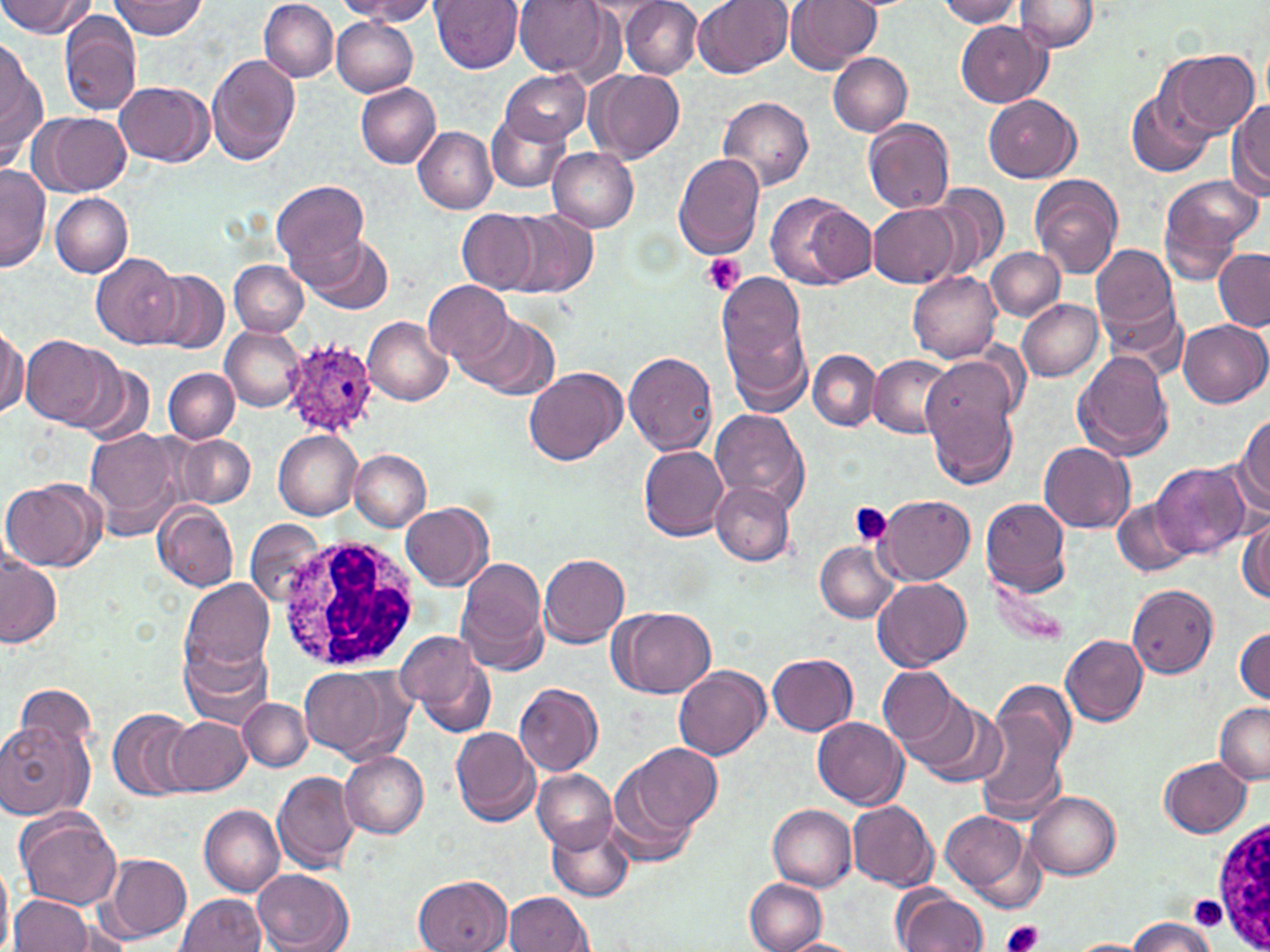

Summary:
  - Coordinate format: approximate bounding boxes as (x1, y1, x2, y2) in pixels
  - Plasmodium ovale-infected red blood cell locations: (283, 340, 379, 435)
  - Uninfected red blood cell locations: (0, 0, 93, 38), (111, 0, 206, 38), (258, 0, 339, 82), (338, 0, 441, 23), (433, 0, 524, 73), (513, 0, 612, 77), (693, 0, 792, 78), (785, 0, 879, 72), (936, 0, 1024, 27), (621, 1, 703, 79), (1014, 1, 1099, 53), (59, 14, 140, 116), (331, 18, 418, 96), (955, 20, 1051, 107), (1, 40, 46, 164), (1162, 50, 1260, 138), (207, 52, 301, 165), (827, 53, 912, 136), (498, 69, 590, 146), (587, 69, 685, 164), (115, 81, 213, 167), (356, 83, 441, 169), (1126, 88, 1214, 179), (983, 94, 1082, 182), (717, 95, 814, 192), (1228, 100, 1270, 199), (36, 112, 130, 196), (485, 113, 571, 193), (864, 118, 956, 213), (413, 126, 496, 212), (547, 147, 639, 232), (673, 154, 766, 258), (1, 165, 49, 273), (1029, 174, 1124, 278), (1158, 175, 1263, 267), (272, 180, 370, 280), (928, 184, 1008, 278), (765, 192, 868, 290), (49, 193, 133, 277), (868, 204, 961, 289), (457, 209, 539, 293), (507, 211, 598, 298), (307, 235, 394, 316), (1089, 243, 1180, 350), (986, 247, 1065, 320), (1213, 250, 1269, 331), (92, 252, 184, 349), (229, 260, 307, 335), (148, 270, 229, 354), (715, 271, 816, 419), (907, 272, 1002, 362), (423, 280, 516, 368), (1016, 298, 1105, 380), (460, 313, 559, 399), (364, 316, 452, 405), (1179, 320, 1269, 407), (0, 323, 26, 419), (221, 327, 303, 411), (19, 334, 117, 429), (808, 349, 881, 431), (1073, 350, 1174, 460), (623, 352, 719, 455), (924, 354, 1023, 442), (867, 355, 953, 438), (80, 360, 156, 445), (522, 365, 627, 465), (163, 366, 240, 443), (924, 386, 1019, 490), (710, 408, 810, 512), (1234, 413, 1270, 512), (86, 428, 183, 537), (273, 430, 361, 519), (179, 436, 254, 507), (1039, 441, 1136, 533), (639, 446, 728, 542), (349, 449, 429, 531), (1152, 463, 1249, 561), (1, 478, 104, 572), (710, 479, 794, 565), (877, 495, 974, 583), (980, 497, 1073, 596), (1112, 498, 1193, 576), (154, 503, 239, 591), (401, 504, 493, 590), (1237, 515, 1269, 604), (245, 519, 325, 607), (815, 541, 898, 623), (1, 550, 61, 649), (538, 554, 629, 648), (456, 559, 549, 673), (988, 576, 1074, 646), (180, 578, 274, 674), (872, 579, 971, 672), (1125, 585, 1217, 677), (615, 607, 715, 698), (1234, 625, 1269, 706), (396, 630, 496, 736), (1059, 632, 1147, 727), (181, 642, 274, 727), (768, 653, 859, 736), (674, 665, 770, 761), (878, 665, 963, 750), (298, 666, 413, 765), (12, 682, 97, 767), (514, 683, 603, 776), (903, 693, 1007, 788), (973, 693, 1075, 823), (238, 697, 312, 772), (1213, 701, 1270, 782), (108, 708, 196, 800), (166, 716, 252, 795), (813, 717, 909, 809), (1, 720, 90, 818), (451, 726, 540, 827), (622, 743, 721, 835), (340, 751, 429, 838), (1160, 757, 1253, 837), (607, 768, 703, 866), (533, 769, 617, 852), (272, 770, 360, 875), (1025, 792, 1121, 879), (847, 800, 938, 891), (768, 804, 857, 890), (200, 805, 285, 897), (17, 810, 124, 912), (938, 810, 1037, 907), (547, 821, 633, 900), (106, 854, 191, 941), (0, 861, 13, 952), (253, 869, 353, 951), (415, 875, 512, 952), (745, 879, 828, 951), (896, 888, 989, 952), (502, 891, 592, 951), (177, 892, 266, 951), (10, 894, 92, 951), (1124, 916, 1218, 951), (779, 937, 861, 952)
  - Platelet locations: (700, 251, 745, 295), (848, 501, 893, 546), (1190, 896, 1227, 928), (1000, 919, 1043, 952)
  - White blood cell locations: (272, 533, 427, 672), (1211, 818, 1270, 952)
  - Slide-level diagnosis: Plasmodium ovale
  - Stain: May-Grünwald-Giemsa
  - Modality: light microscopy
  - Image size: 1270×952 pixels
  - Magnification: 1000x
  - Field of view: single
  - Preparation: thin blood film